Give the position of every Plasmodium parasite visible.
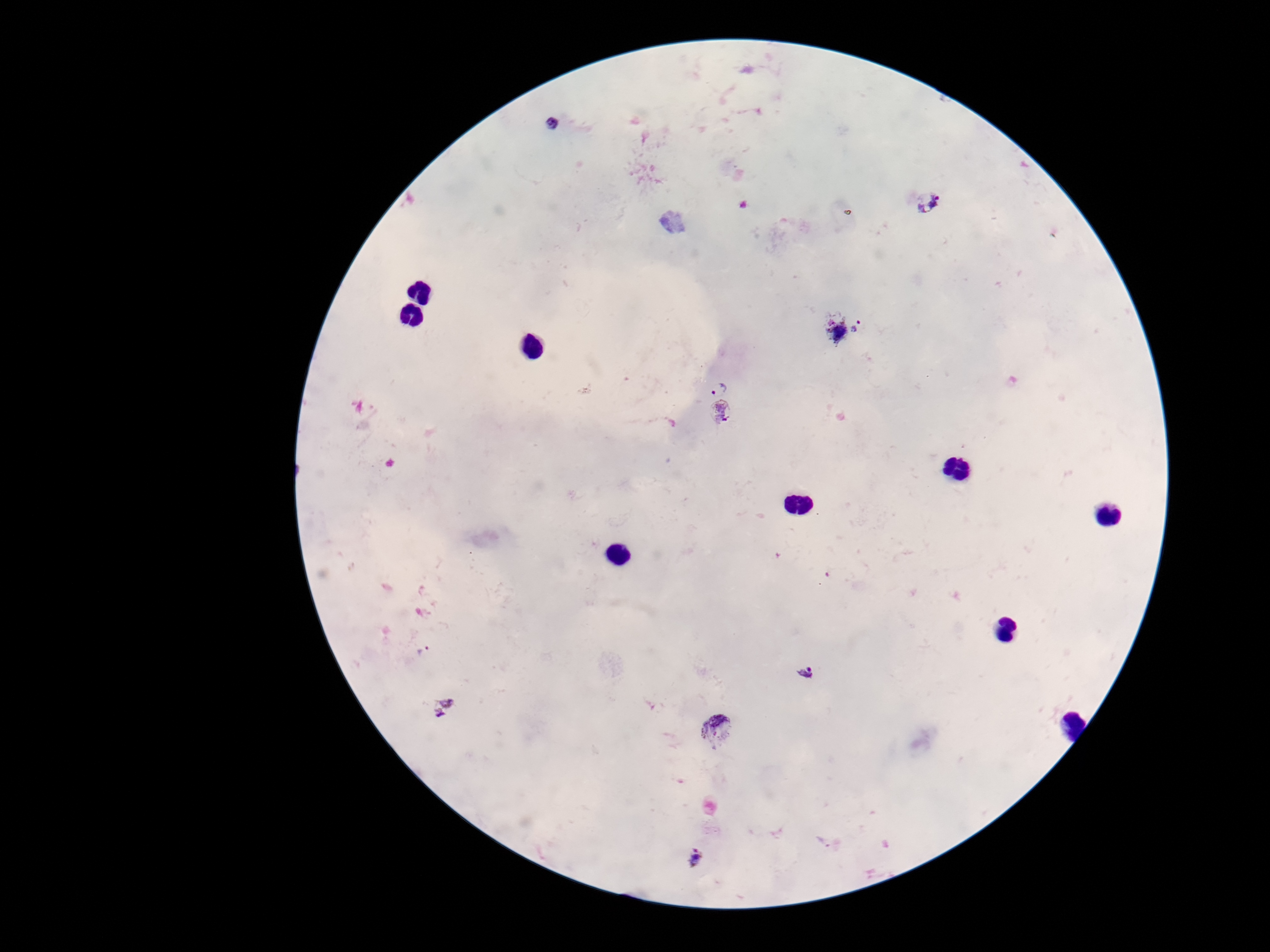
Approximate object centers, in pixels from the top-left corner.
Plasmodium parasites: (x=551, y=124), (x=928, y=202), (x=838, y=332), (x=718, y=387), (x=721, y=414), (x=423, y=651), (x=805, y=672), (x=442, y=709), (x=717, y=731), (x=697, y=860).

preparation: thick peripheral-blood smear
field_of_view: single
image_size: 1270×952 pixels
patient_malaria_status: positive
stain: Giemsa
magnification: 100x
capture: smartphone camera through the microscope eyepiece